Assess this cell for malaria.
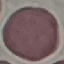

It is uninfected.

Summary:
  - Preparation: thin blood film
  - Capture: smartphone camera at the microscope eyepiece
  - Image type: cell patch, automatically extracted from a larger field of view and resized to 64 × 64 pixels
  - Stain: Giemsa